Assess this cell for malaria.
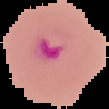
It is parasitized.

preparation = thin blood film
image type = segmented cell region on a black background
image size = 109×109 pixels